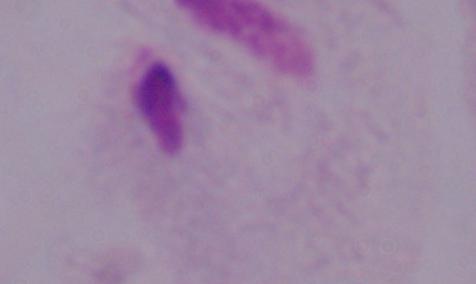

Summary:
  - Identification: trichomonad
  - Magnification: 1000x
  - Modality: micrograph